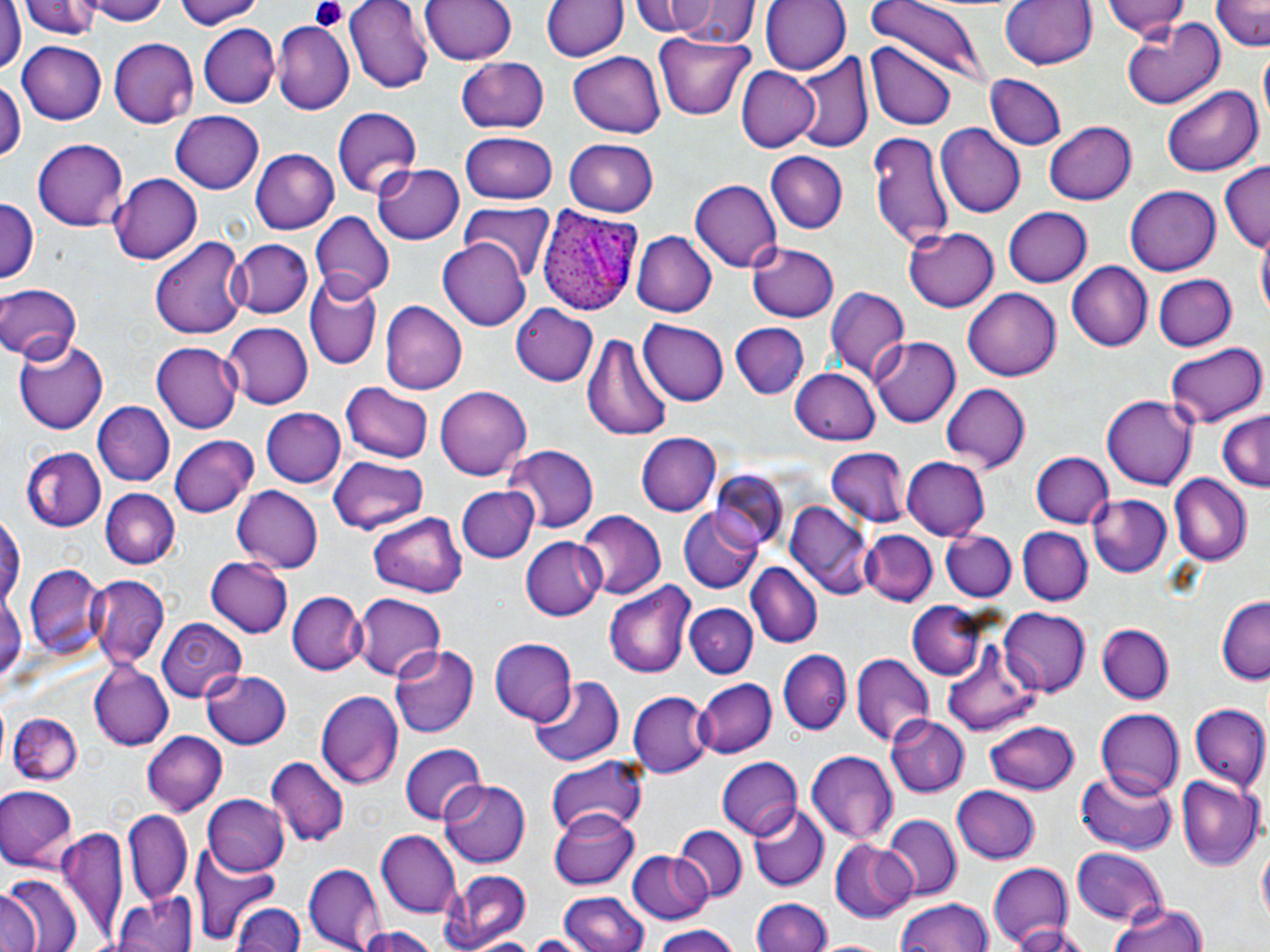

Summary:
  - Coordinate format: approximate bounding boxes as [x1, y1, x2, y2] in pixels
  - Plasmodium ovale-infected red blood cell locations: [535, 203, 642, 317]
  - Uninfected red blood cell locations: [21, 0, 98, 39], [79, 0, 168, 24], [345, 0, 435, 93], [418, 0, 518, 65], [631, 0, 714, 36], [652, 0, 757, 49], [760, 0, 848, 75], [865, 0, 984, 89], [997, 0, 1097, 72], [1102, 0, 1195, 40], [175, 1, 264, 31], [543, 1, 627, 64], [1212, 1, 1268, 53], [1, 4, 25, 73], [1120, 18, 1225, 113], [271, 20, 353, 114], [199, 25, 278, 107], [653, 34, 754, 120], [108, 37, 198, 128], [17, 42, 107, 124], [868, 42, 957, 129], [568, 51, 665, 139], [793, 52, 873, 155], [456, 56, 550, 134], [737, 66, 820, 151], [985, 74, 1066, 152], [0, 77, 24, 170], [1161, 83, 1263, 179], [330, 106, 421, 198], [171, 110, 262, 192], [1044, 122, 1135, 205], [935, 124, 1026, 218], [867, 131, 955, 249], [459, 132, 559, 205], [32, 138, 130, 230], [564, 138, 659, 217], [250, 147, 339, 233], [766, 152, 846, 234], [373, 160, 464, 244], [1217, 163, 1270, 253], [107, 171, 202, 267], [690, 178, 782, 271], [1126, 185, 1222, 275], [0, 198, 38, 282], [460, 202, 558, 281], [1001, 206, 1090, 287], [311, 212, 394, 298], [902, 225, 1000, 312], [631, 230, 715, 317], [438, 235, 531, 328], [151, 236, 248, 340], [1258, 237, 1269, 324], [230, 239, 312, 319], [746, 239, 841, 323], [1068, 262, 1152, 351], [1153, 273, 1237, 353], [304, 276, 381, 371], [0, 281, 83, 363], [823, 285, 911, 384], [964, 289, 1060, 380], [380, 300, 465, 395], [511, 303, 600, 387], [639, 319, 730, 406], [223, 322, 313, 409], [730, 322, 809, 399], [584, 328, 673, 444], [868, 336, 959, 427], [15, 338, 110, 432], [1165, 340, 1267, 428], [154, 343, 241, 432], [789, 366, 881, 443], [941, 383, 1031, 472], [341, 384, 434, 464], [434, 385, 532, 482], [1103, 395, 1195, 491], [92, 401, 174, 484], [262, 409, 346, 487], [1217, 409, 1270, 492], [634, 433, 720, 516], [170, 434, 259, 518], [503, 446, 597, 535], [23, 447, 108, 532], [825, 449, 910, 529], [1030, 450, 1113, 527], [901, 455, 991, 541], [327, 457, 430, 533], [711, 473, 790, 552], [1170, 475, 1252, 564], [232, 485, 323, 573], [456, 485, 538, 563], [102, 489, 177, 569], [1089, 494, 1174, 579], [785, 500, 873, 597], [678, 507, 764, 593], [576, 512, 666, 601], [367, 513, 467, 597], [0, 515, 24, 610], [1016, 526, 1092, 606], [860, 530, 936, 608], [941, 530, 1016, 602], [521, 536, 606, 622], [205, 556, 292, 638], [746, 563, 822, 648], [25, 565, 103, 659], [87, 574, 170, 671], [606, 581, 697, 679], [0, 583, 25, 693], [288, 591, 365, 675], [351, 592, 448, 680], [1217, 596, 1270, 683], [907, 602, 996, 683], [685, 603, 758, 679], [998, 607, 1089, 695], [158, 619, 245, 704], [1095, 622, 1174, 703], [941, 634, 1043, 736], [487, 636, 576, 723], [391, 643, 479, 738], [778, 648, 851, 735], [851, 654, 933, 746], [90, 663, 172, 750], [201, 668, 292, 748], [529, 676, 624, 770], [694, 678, 776, 759], [316, 688, 402, 791], [630, 691, 710, 776], [1187, 704, 1269, 791], [1095, 709, 1185, 800], [13, 714, 83, 785], [884, 715, 968, 797], [985, 718, 1082, 792], [142, 729, 227, 814], [399, 744, 486, 826], [805, 748, 899, 843], [265, 757, 349, 849], [718, 757, 803, 838], [546, 759, 647, 839], [1076, 769, 1177, 854], [1176, 775, 1264, 870], [438, 779, 529, 868], [0, 785, 76, 869], [951, 786, 1040, 865], [202, 794, 290, 877], [748, 804, 827, 891], [549, 808, 640, 887], [121, 812, 191, 903], [883, 814, 961, 898], [674, 825, 745, 901], [56, 829, 128, 943], [376, 831, 461, 917], [825, 838, 917, 923], [1258, 844, 1269, 928], [1071, 845, 1169, 924], [627, 851, 713, 926], [192, 853, 284, 942], [986, 862, 1075, 950], [304, 863, 384, 950], [439, 869, 533, 951], [2, 875, 80, 952], [560, 890, 647, 952], [113, 891, 196, 952], [0, 893, 40, 952], [752, 897, 829, 952], [895, 897, 994, 952], [232, 902, 303, 952], [1109, 903, 1209, 952], [1010, 923, 1096, 952], [356, 924, 437, 952], [648, 925, 741, 952], [467, 934, 545, 952], [517, 935, 593, 952], [816, 939, 893, 952]
  - Platelet locations: [311, 0, 349, 33]
  - Slide-level diagnosis: Plasmodium ovale
  - Field of view: single
  - Modality: light microscopy
  - Image size: 1270×952 pixels
  - Preparation: thin blood film
  - Stain: May-Grünwald-Giemsa
  - Magnification: 1000x